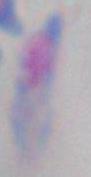
1000x magnification. Toxoplasma gondii is seen. Micrograph.